Name the parasite shown.
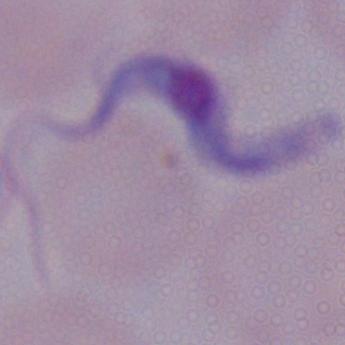
A trypanosome.

Summary:
  - Magnification: 1000x
  - Modality: photomicrograph